Outline each blood parasite and name the species.
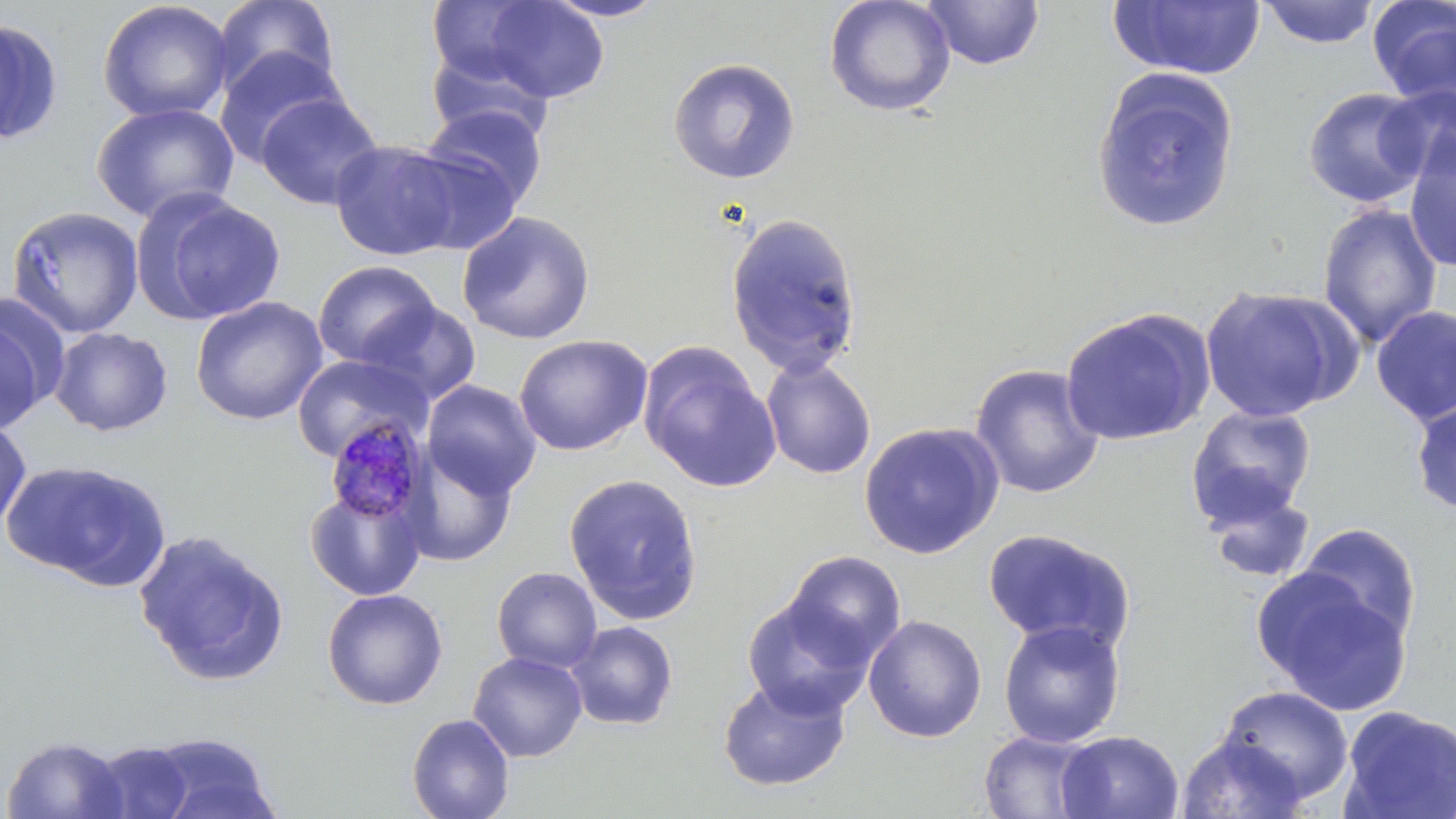

Approximate bounding boxes as [x1, y1, x2, y2] in pixels.
Plasmodium malariae-infected red blood cells: [325, 418, 433, 527].
No Plasmodium falciparum, Plasmodium ovale, Plasmodium vivax, Babesia divergens, or Trypanosoma brucei observed.

Uninfected red blood cell locations: [210, 0, 341, 100], [542, 0, 670, 22], [824, 0, 956, 117], [97, 1, 234, 123], [475, 1, 612, 104], [921, 1, 1046, 71], [1108, 1, 1267, 81], [1258, 1, 1380, 49], [1367, 1, 1456, 109], [425, 2, 547, 86], [0, 17, 63, 145], [426, 42, 556, 144], [214, 47, 346, 168], [668, 57, 800, 183], [1091, 68, 1240, 233], [1377, 84, 1456, 188], [1303, 87, 1432, 208], [255, 92, 384, 211], [91, 101, 241, 223], [423, 103, 548, 213], [1403, 132, 1456, 273], [329, 139, 464, 262], [405, 149, 522, 255], [132, 189, 287, 326], [1317, 204, 1443, 349], [6, 206, 145, 339], [457, 211, 596, 345], [725, 211, 863, 378], [312, 260, 440, 369], [1199, 285, 1353, 422], [190, 296, 328, 425], [358, 300, 482, 406], [1371, 304, 1456, 427], [0, 306, 57, 434], [1059, 307, 1216, 447], [49, 326, 173, 436], [514, 334, 653, 456], [637, 341, 781, 494], [292, 354, 429, 462], [761, 357, 877, 480], [969, 363, 1106, 499], [422, 379, 542, 500], [1410, 397, 1456, 517], [1185, 404, 1316, 527], [0, 417, 32, 533], [859, 421, 1004, 560], [401, 447, 518, 568], [2, 460, 170, 590], [563, 473, 704, 625], [1202, 482, 1318, 586], [304, 484, 428, 601], [1296, 523, 1421, 647], [983, 527, 1134, 654], [133, 530, 291, 686], [783, 551, 906, 667], [492, 567, 602, 673], [1252, 568, 1412, 714], [321, 588, 448, 710], [742, 596, 875, 719], [863, 615, 987, 742], [997, 619, 1126, 748], [565, 621, 679, 731], [468, 651, 588, 762], [717, 676, 851, 792], [1218, 685, 1354, 805], [1338, 705, 1456, 819], [407, 713, 515, 819], [977, 729, 1103, 818], [1056, 730, 1184, 818], [145, 732, 279, 819], [1176, 734, 1307, 818], [1, 735, 128, 818], [87, 740, 197, 819]. Slide-level diagnosis: Plasmodium malariae. May-Grünwald-Giemsa-stained preparation. 1000x magnification. Single field of view. Thin blood smear. Image is 1456×819 pixels. Light microscopy.